Identify the preparation type.
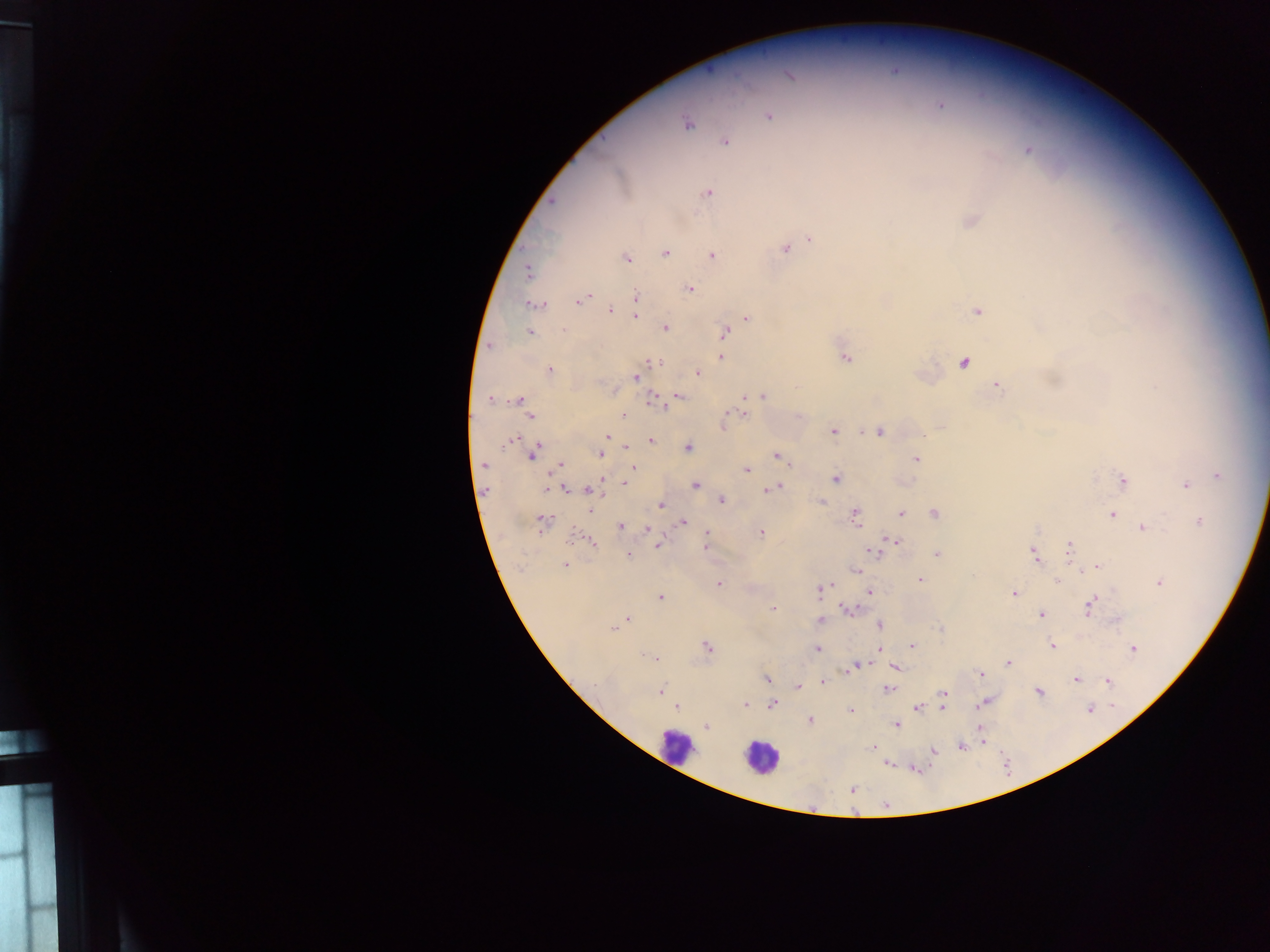
Thick blood film.

Approximate centers as {x, y} in pixels.
Summary:
  - Plasmodium parasite locations: {940, 105}, {768, 116}, {687, 124}, {725, 142}, {1028, 150}, {708, 193}, {971, 221}, {810, 240}, {785, 249}, {665, 253}, {712, 255}, {625, 257}, {528, 272}, {688, 289}, {635, 296}, {584, 297}, {579, 301}, {634, 303}, {533, 305}, {610, 310}, {977, 311}, {636, 316}, {746, 318}, {665, 327}, {564, 330}, {530, 333}, {724, 333}, {721, 357}, {845, 358}, {654, 362}, {964, 362}, {550, 371}, {698, 373}, {636, 377}, {997, 386}, {1156, 387}, {763, 396}, {679, 397}, {744, 398}, {490, 399}, {519, 400}, {655, 401}, {744, 414}, {622, 415}, {529, 416}, {723, 426}, {941, 427}, {833, 431}, {879, 432}, {607, 437}, {513, 440}, {651, 441}, {626, 445}, {688, 448}, {533, 453}, {600, 454}, {776, 456}, {916, 459}, {484, 465}, {560, 466}, {633, 468}, {747, 469}, {1218, 475}, {836, 479}, {1123, 480}, {626, 481}, {696, 485}, {1186, 485}, {778, 487}, {565, 489}, {769, 489}, {590, 490}, {721, 500}, {822, 502}, {661, 506}, {590, 509}, {934, 513}, {901, 514}, {854, 515}, {1112, 515}, {683, 522}, {1199, 522}, {543, 523}, {621, 526}, {1142, 528}, {649, 529}, {762, 532}, {707, 533}, {893, 541}, {591, 542}, {657, 545}, {705, 549}, {1069, 550}, {872, 551}, {937, 554}, {1034, 554}, {629, 556}, {565, 564}, {1097, 566}, {1085, 569}, {855, 571}, {920, 580}, {1056, 581}, {1158, 583}, {719, 584}, {829, 585}, {822, 589}, {870, 592}, {1014, 593}, {661, 596}, {1090, 606}, {773, 609}, {848, 610}, {1041, 614}, {627, 619}, {821, 620}, {879, 626}, {613, 629}, {707, 646}, {912, 646}, {1052, 646}, {817, 648}, {879, 649}, {1133, 649}, {653, 658}, {1008, 663}, {853, 666}, {895, 668}, {981, 674}, {767, 679}, {1076, 680}, {1108, 681}, {823, 682}, {596, 684}, {798, 686}, {887, 689}, {661, 690}, {1039, 692}, {944, 694}, {983, 703}, {745, 704}, {773, 704}, {677, 706}, {941, 707}, {917, 708}, {1091, 708}, {850, 712}, {810, 720}, {897, 724}, {706, 727}, {982, 738}, {874, 747}, {961, 747}, {934, 750}, {852, 790}
  - Leukocyte locations: {675, 746}, {759, 757}
  - Image size: 1270×952 pixels
  - Field of view: single
  - Capture: mobile-phone photograph through a microscope
  - Country: Ghana